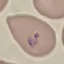
Summary:
  - Malaria status: parasitized
  - Stain: Giemsa
  - Preparation: thin blood film
  - Image type: cell patch, automatically extracted from a larger field of view and resized to 64 × 64 pixels
  - Capture: smartphone camera at the microscope eyepiece